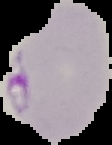

From a thin blood smear. Image is 112×145 pixels. Segmented cell region on a black background. Malaria status: parasitized.